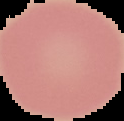
Segmented cell region on a black background. From a thin blood film. Result: no Plasmodium parasites detected. Image is 124×121 pixels.